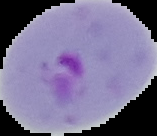
image size = 157×136 pixels
preparation = thin blood smear
image type = cell region segmented out of the field of view; surrounding area masked to black
malaria status = parasitized